Describe the morphology of the red blood cells.
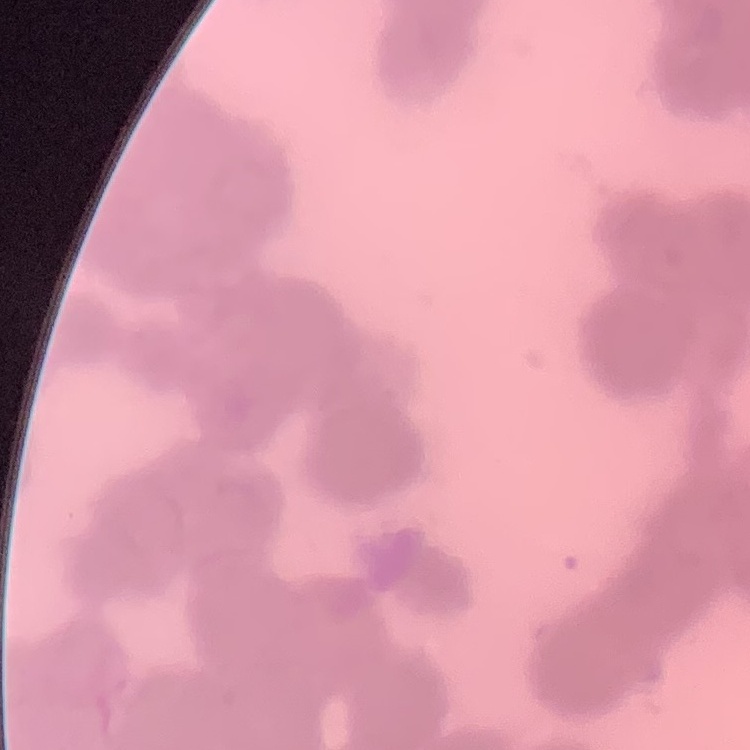

Rouleaux formation.

Summary:
  - Stain: Field's or Giemsa
  - Preparation: thin peripheral smear
  - Image type: one tile cut from a larger photomicrograph